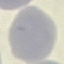 Malaria status: uninfected. Acquired by smartphone through the microscope eyepiece. Giemsa-stained preparation. Thin blood film. Cell patch, automatically extracted from a larger field of view and resized to 64 × 64 pixels.